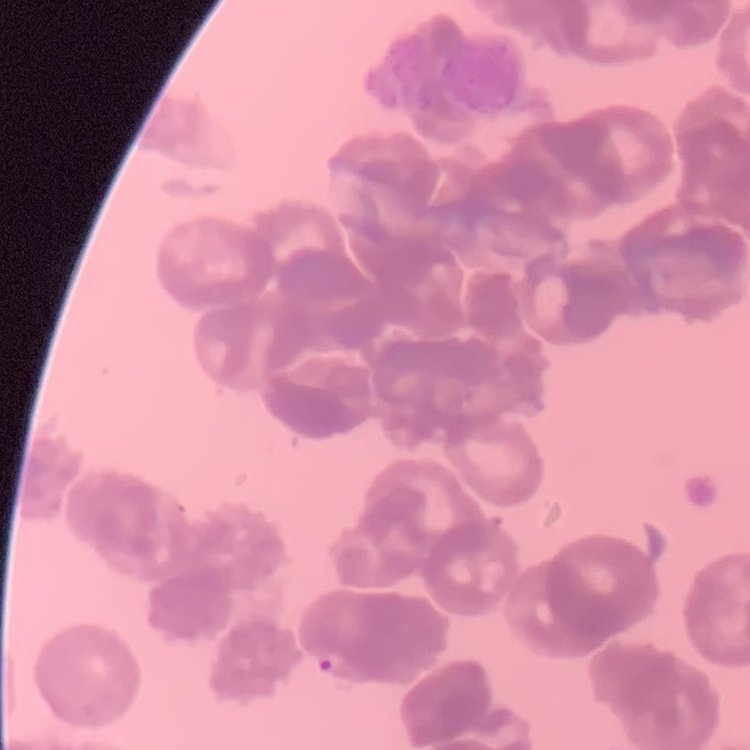
Summary:
  - Red blood cell morphology: rouleaux formation
  - Stain: Field's or Giemsa
  - Preparation: thin blood smear
  - Image type: one tile cut from a larger photomicrograph